Give the position of every Plasmodium parasite.
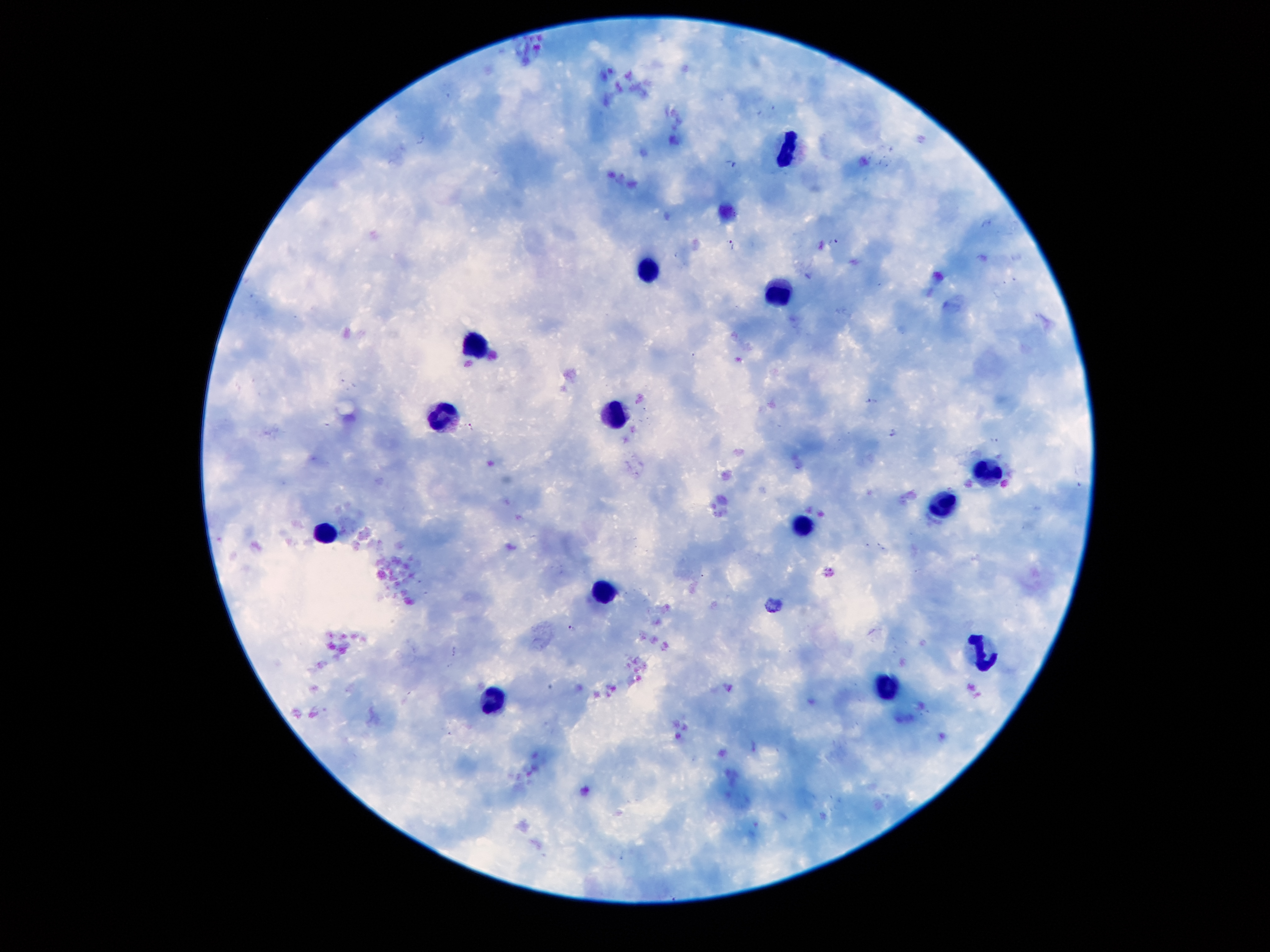
Approximate centers as (x, y) in pixels.
Plasmodium parasites: (732, 163), (729, 242), (831, 242), (872, 401), (470, 426), (894, 433), (571, 628).

Leukocyte locations: (788, 146), (651, 273), (783, 296), (476, 343), (617, 414), (441, 418), (984, 470), (942, 506), (803, 521), (329, 534), (602, 594), (986, 650), (894, 690), (491, 705). Giemsa-stained preparation. Patient malaria status: infected with Plasmodium falciparum. Photographed through the microscope eyepiece with a smartphone camera. 100x magnification. Single field of view. Image is 1270×952 pixels. Thick blood film.